Assess this cell for malaria.
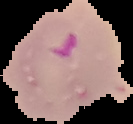

Parasitized.

Image is 133×124 pixels. The area outside the segmented cell region is set to black. From a thin blood film.